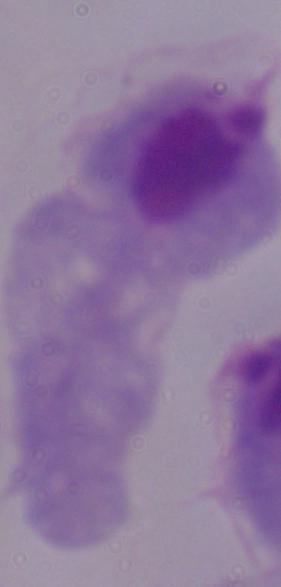

Summary:
  - Identification: trichomonad
  - Magnification: 1000x
  - Modality: photomicrograph